Outline each blood parasite and name the species.
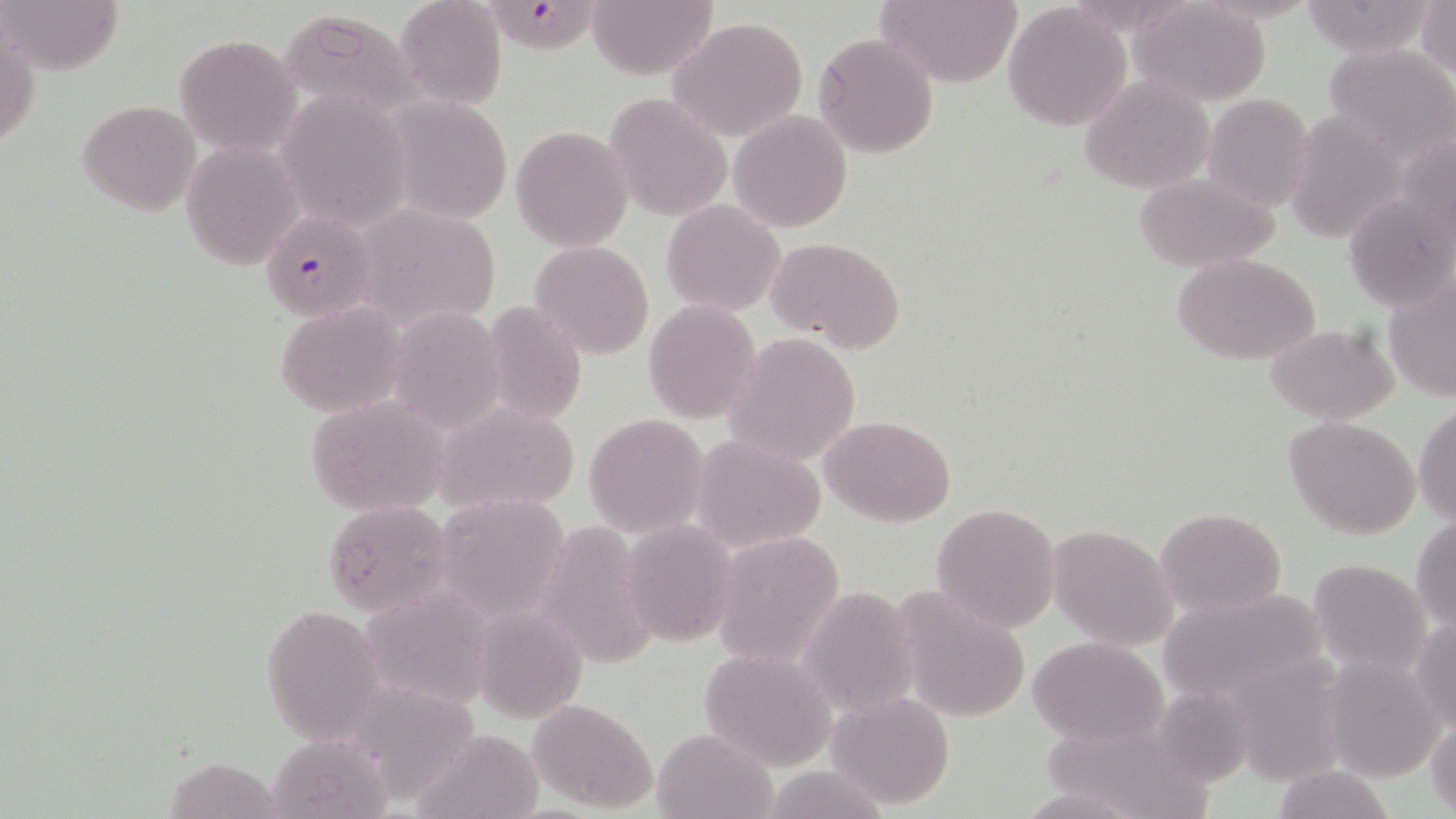

Approximate bounding boxes as named x1/y1/x2/y2 corners in pixels.
Plasmodium falciparum-infected red blood cells: (x1=487, y1=4, x2=606, y2=59), (x1=261, y1=213, x2=374, y2=320).
No Plasmodium ovale, Plasmodium malariae, Plasmodium vivax, Babesia divergens, or Trypanosoma brucei observed.

Summary:
  - Uninfected red blood cell locations: (x1=1, y1=0, x2=122, y2=74), (x1=394, y1=0, x2=508, y2=111), (x1=586, y1=0, x2=718, y2=79), (x1=874, y1=0, x2=1023, y2=88), (x1=1418, y1=1, x2=1455, y2=86), (x1=1128, y1=2, x2=1273, y2=107), (x1=1003, y1=5, x2=1133, y2=131), (x1=279, y1=9, x2=420, y2=117), (x1=666, y1=17, x2=809, y2=144), (x1=1, y1=18, x2=39, y2=151), (x1=174, y1=32, x2=302, y2=158), (x1=812, y1=32, x2=939, y2=159), (x1=1323, y1=42, x2=1456, y2=160), (x1=1080, y1=75, x2=1213, y2=195), (x1=277, y1=89, x2=411, y2=232), (x1=606, y1=92, x2=732, y2=221), (x1=1202, y1=95, x2=1317, y2=208), (x1=78, y1=100, x2=202, y2=216), (x1=727, y1=110, x2=853, y2=232), (x1=512, y1=125, x2=634, y2=251), (x1=179, y1=142, x2=303, y2=268), (x1=1133, y1=171, x2=1279, y2=271), (x1=661, y1=199, x2=785, y2=316), (x1=351, y1=202, x2=503, y2=336), (x1=766, y1=236, x2=906, y2=353), (x1=528, y1=240, x2=656, y2=359), (x1=1173, y1=252, x2=1321, y2=366), (x1=1383, y1=278, x2=1455, y2=403), (x1=642, y1=299, x2=762, y2=422), (x1=276, y1=300, x2=408, y2=417), (x1=482, y1=302, x2=587, y2=426), (x1=384, y1=308, x2=508, y2=429), (x1=1265, y1=323, x2=1398, y2=423), (x1=723, y1=331, x2=862, y2=466), (x1=305, y1=394, x2=450, y2=517), (x1=429, y1=397, x2=582, y2=517), (x1=1414, y1=400, x2=1455, y2=527), (x1=583, y1=413, x2=709, y2=536), (x1=1284, y1=415, x2=1422, y2=539), (x1=821, y1=416, x2=955, y2=526), (x1=689, y1=435, x2=825, y2=551), (x1=433, y1=493, x2=571, y2=625), (x1=324, y1=500, x2=455, y2=616), (x1=931, y1=501, x2=1061, y2=633), (x1=1156, y1=506, x2=1286, y2=618), (x1=1412, y1=515, x2=1456, y2=635), (x1=536, y1=521, x2=658, y2=671), (x1=620, y1=521, x2=737, y2=645), (x1=1049, y1=524, x2=1177, y2=649), (x1=711, y1=532, x2=845, y2=668), (x1=1307, y1=558, x2=1432, y2=674), (x1=1157, y1=585, x2=1332, y2=704), (x1=799, y1=586, x2=919, y2=719), (x1=891, y1=587, x2=1032, y2=723), (x1=258, y1=603, x2=386, y2=743), (x1=1411, y1=618, x2=1456, y2=734), (x1=1028, y1=635, x2=1170, y2=745), (x1=699, y1=646, x2=839, y2=771), (x1=1321, y1=651, x2=1448, y2=780), (x1=826, y1=689, x2=954, y2=809), (x1=526, y1=698, x2=658, y2=811), (x1=1427, y1=718, x2=1456, y2=815), (x1=652, y1=728, x2=775, y2=818), (x1=410, y1=732, x2=546, y2=819), (x1=162, y1=757, x2=290, y2=818), (x1=760, y1=763, x2=894, y2=819)
  - Slide-level diagnosis: Plasmodium falciparum
  - Field of view: one of a larger specimen
  - Stain: May-Grünwald-Giemsa
  - Preparation: thin blood film
  - Modality: light microscopy
  - Magnification: 1000x
  - Image size: 1456×819 pixels